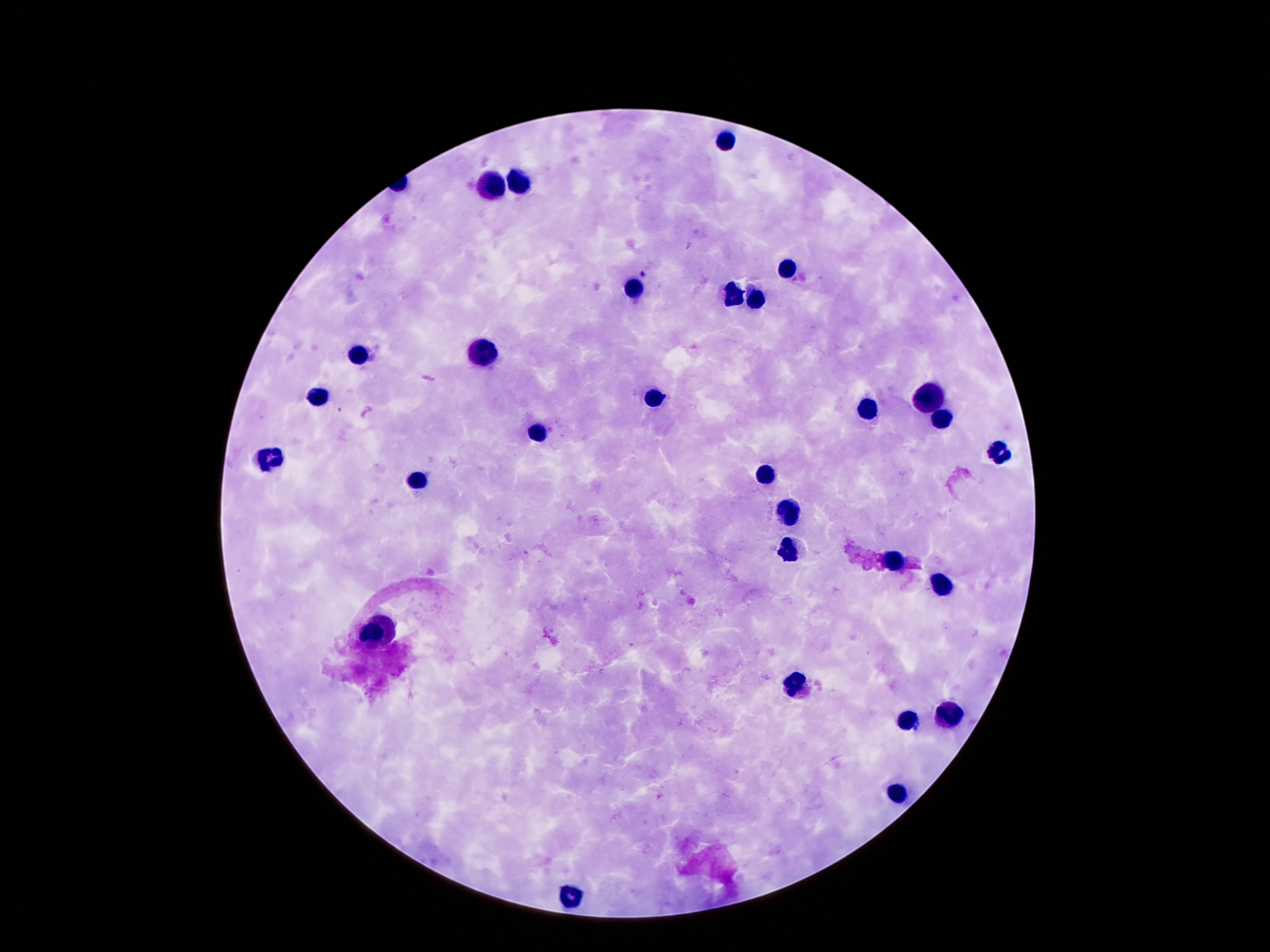 Approximate object centers, in pixels from the top-left corner. Leukocyte locations: (x=725, y=142), (x=521, y=183), (x=492, y=185), (x=789, y=266), (x=634, y=288), (x=736, y=296), (x=758, y=301), (x=477, y=353), (x=360, y=356), (x=318, y=394), (x=654, y=397), (x=930, y=397), (x=868, y=408), (x=939, y=419), (x=534, y=432), (x=1001, y=452), (x=267, y=460), (x=764, y=477), (x=415, y=481), (x=788, y=512), (x=786, y=551), (x=892, y=561), (x=941, y=586), (x=377, y=633), (x=793, y=682), (x=950, y=716), (x=908, y=722), (x=897, y=791), (x=574, y=895). Thick blood film. Patient malaria status: negative. Single field of view. Photographed through the microscope eyepiece with a smartphone camera. 100x magnification. Giemsa stain. Image is 1270×952 pixels.